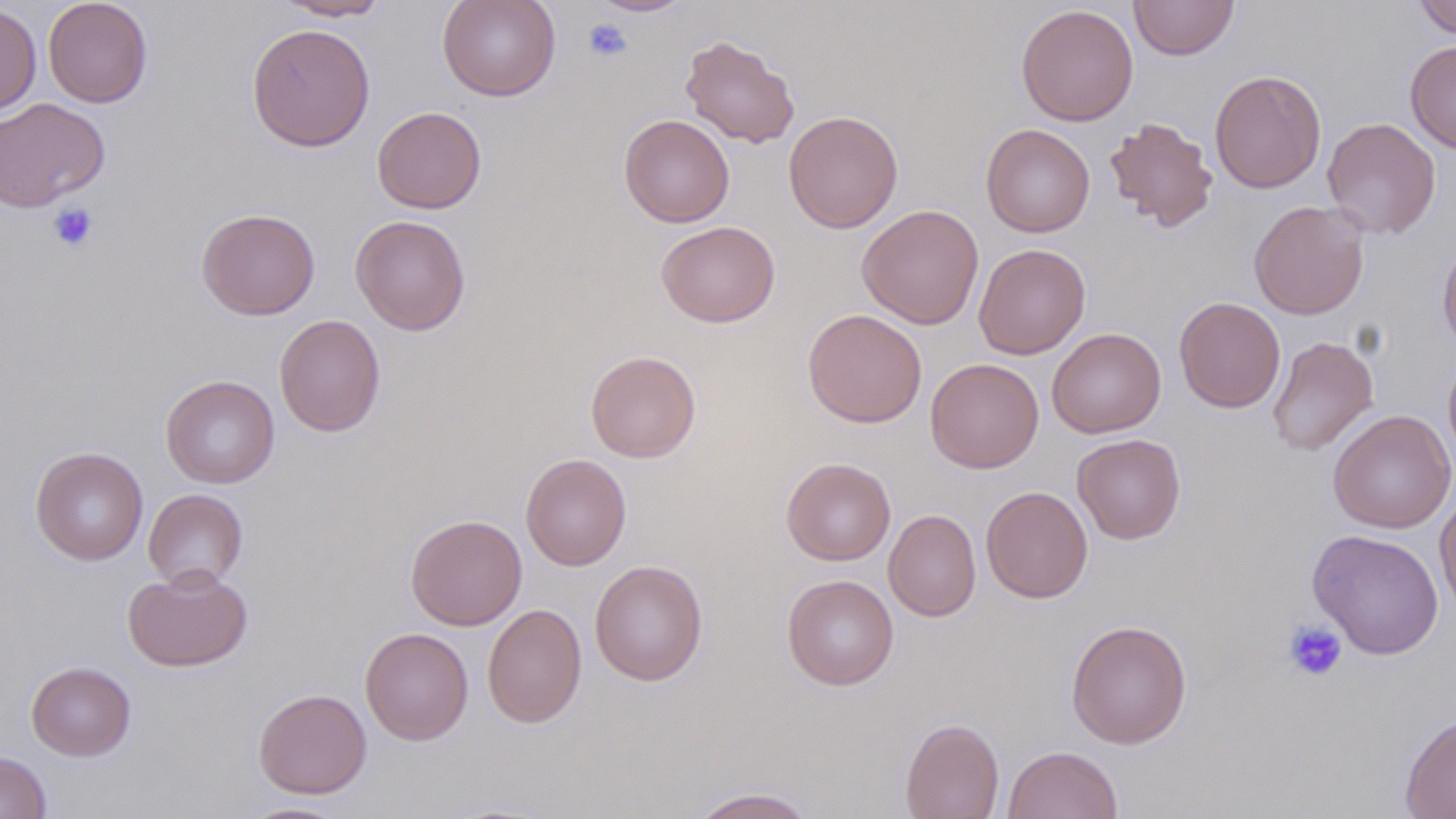
Summary:
  - Coordinate format: approximate bounding boxes as (x1, y1, x2, y2) in pixels
  - Platelet locations: (583, 18, 633, 62), (48, 202, 99, 252), (1282, 620, 1347, 682)
  - Uninfected red blood cell locations: (43, 0, 153, 108), (273, 0, 393, 21), (437, 0, 561, 102), (587, 0, 695, 17), (1129, 0, 1239, 60), (1413, 0, 1456, 39), (0, 3, 42, 116), (1015, 4, 1138, 126), (247, 23, 375, 151), (680, 34, 801, 148), (1405, 40, 1456, 154), (1210, 69, 1327, 194), (0, 98, 110, 212), (371, 106, 487, 214), (784, 110, 903, 233), (619, 114, 735, 227), (1104, 116, 1219, 232), (1322, 117, 1440, 238), (980, 123, 1095, 238), (1249, 200, 1370, 320), (857, 204, 984, 329), (196, 207, 320, 320), (350, 214, 471, 335), (656, 221, 781, 327), (1437, 237, 1456, 356), (973, 243, 1091, 360), (1174, 296, 1285, 413), (803, 309, 927, 428), (274, 314, 386, 437), (1047, 328, 1166, 438), (1267, 336, 1378, 456), (586, 350, 701, 463), (1443, 350, 1456, 471), (925, 357, 1044, 473), (160, 374, 280, 489), (1327, 409, 1455, 534), (1072, 433, 1186, 544), (30, 446, 148, 565), (520, 452, 631, 570), (781, 457, 896, 566), (980, 486, 1093, 603), (143, 488, 248, 591), (1435, 488, 1456, 620), (883, 509, 981, 622), (406, 515, 527, 630), (1307, 528, 1444, 659), (590, 559, 708, 686), (122, 565, 253, 672), (782, 574, 899, 690), (482, 603, 587, 728), (1066, 619, 1192, 749), (359, 627, 473, 745), (26, 661, 136, 761), (253, 688, 372, 799), (1399, 712, 1456, 819), (900, 718, 1004, 819), (1002, 745, 1124, 819), (0, 752, 51, 819), (687, 786, 816, 818), (238, 801, 353, 818)
  - Slide-level diagnosis: negative for blood parasites
  - Field of view: single
  - Modality: optical microscopy
  - Preparation: thin blood film
  - Magnification: 1000x
  - Stain: May-Grünwald-Giemsa
  - Image size: 1456×819 pixels